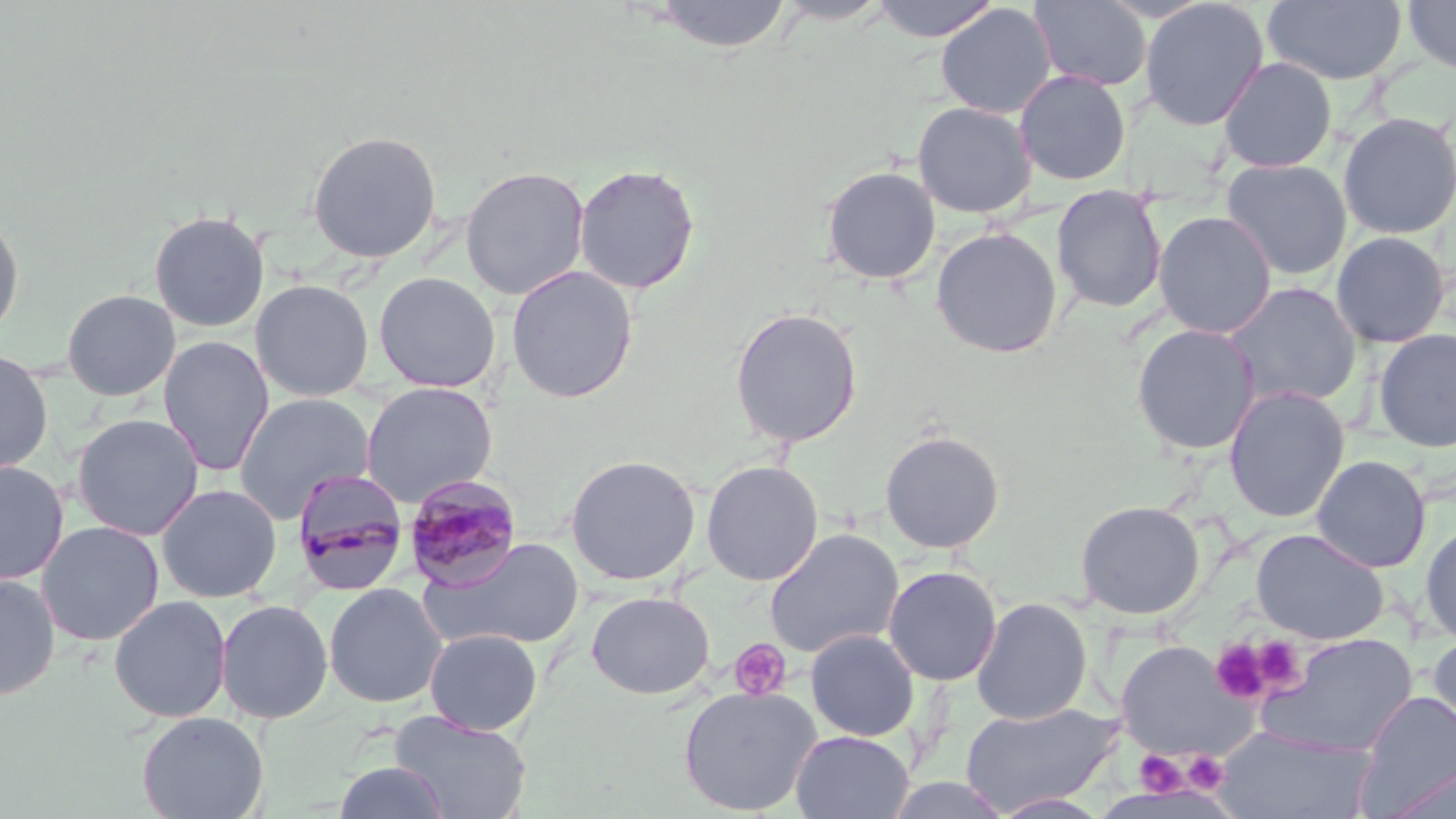

slide-level diagnosis = Plasmodium malariae
field of view = single
magnification = 1000x
preparation = thin blood film
modality = optical microscopy
uninfected red blood cell locations (subset) = approximate bounding boxes as (x1,y1)-(x2,y2) corner pairs in pixels: (645,0)-(793,53), (774,0)-(894,25), (869,0)-(1000,42), (1030,0)-(1152,92), (1139,0)-(1269,131), (1263,0)-(1408,86), (1402,0)-(1456,76), (935,3)-(1057,119), (1217,56)-(1338,173), (1014,70)-(1132,186), (912,101)-(1037,218), (1337,111)-(1456,240), (307,130)-(442,263), (1221,158)-(1353,280), (573,163)-(701,295), (460,165)-(590,300), (821,166)-(941,285), (1051,185)-(1168,313), (0,209)-(25,342), (148,209)-(269,333), (1153,210)-(1276,339), (930,227)-(1063,358), (1330,230)-(1452,349), (506,265)-(638,404), (374,271)-(501,393), (250,279)-(374,401), (1222,282)-(1362,410), (61,289)-(181,400), (729,307)-(864,448), (1131,323)-(1260,455), (1373,328)-(1456,452), (158,336)-(274,477), (0,349)-(53,474), (361,382)-(497,507), (1223,385)-(1350,523), (234,393)-(374,524), (72,413)-(204,541), (879,430)-(1005,554), (1311,454)-(1431,573), (565,455)-(701,585), (701,459)-(823,586), (0,461)-(69,585), (156,483)-(282,603), (1075,499)-(1205,619), (36,520)-(164,646), (1419,521)-(1456,645), (1251,527)-(1389,644), (764,528)-(904,659), (420,537)-(586,651), (882,565)-(1002,686), (0,572)-(60,701), (323,582)-(447,708), (586,591)-(714,699), (109,595)-(232,723), (971,597)-(1093,725), (215,599)-(334,724), (425,628)-(542,735), (805,628)-(920,741), (1257,632)-(1418,758), (1426,632)-(1456,747), (1115,640)-(1249,759), (677,684)-(823,816), (1356,691)-(1456,814), (958,701)-(1123,815), (389,710)-(532,819), (136,711)-(268,819), (1214,728)-(1379,818), (790,730)-(914,819), (333,760)-(450,818), (1380,762)-(1456,819), (991,793)-(1113,818)
stain = May-Grünwald-Giemsa
image size = 1456×819 pixels
platelet locations = approximate bounding boxes as (x1,y1)-(x2,y2) corner pairs in pixels: (1252,636)-(1305,692), (728,638)-(792,701), (1209,638)-(1273,706), (1135,751)-(1186,796), (1183,752)-(1229,794)
Plasmodium malariae-infected red blood cell locations (subset) = approximate bounding boxes as (x1,y1)-(x2,y2) corner pairs in pixels: (404,474)-(524,590)